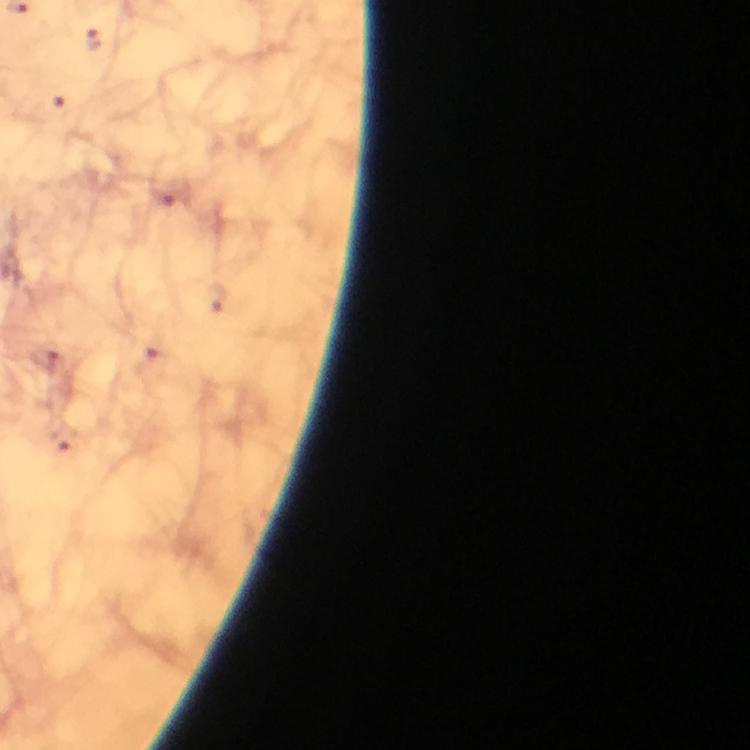
Approximate object centers, in pixels from the top-left corner. Plasmodium parasite locations: (x=93, y=39), (x=57, y=100), (x=164, y=196), (x=47, y=360), (x=151, y=362). From a malaria diagnostic workup. Cropped region of a single field of view. Thick smear. Image is 750×750 pixels. Immersion oil was used. Giemsa-stained preparation. 100x magnification. Photographed with a smartphone mounted on the microscope.